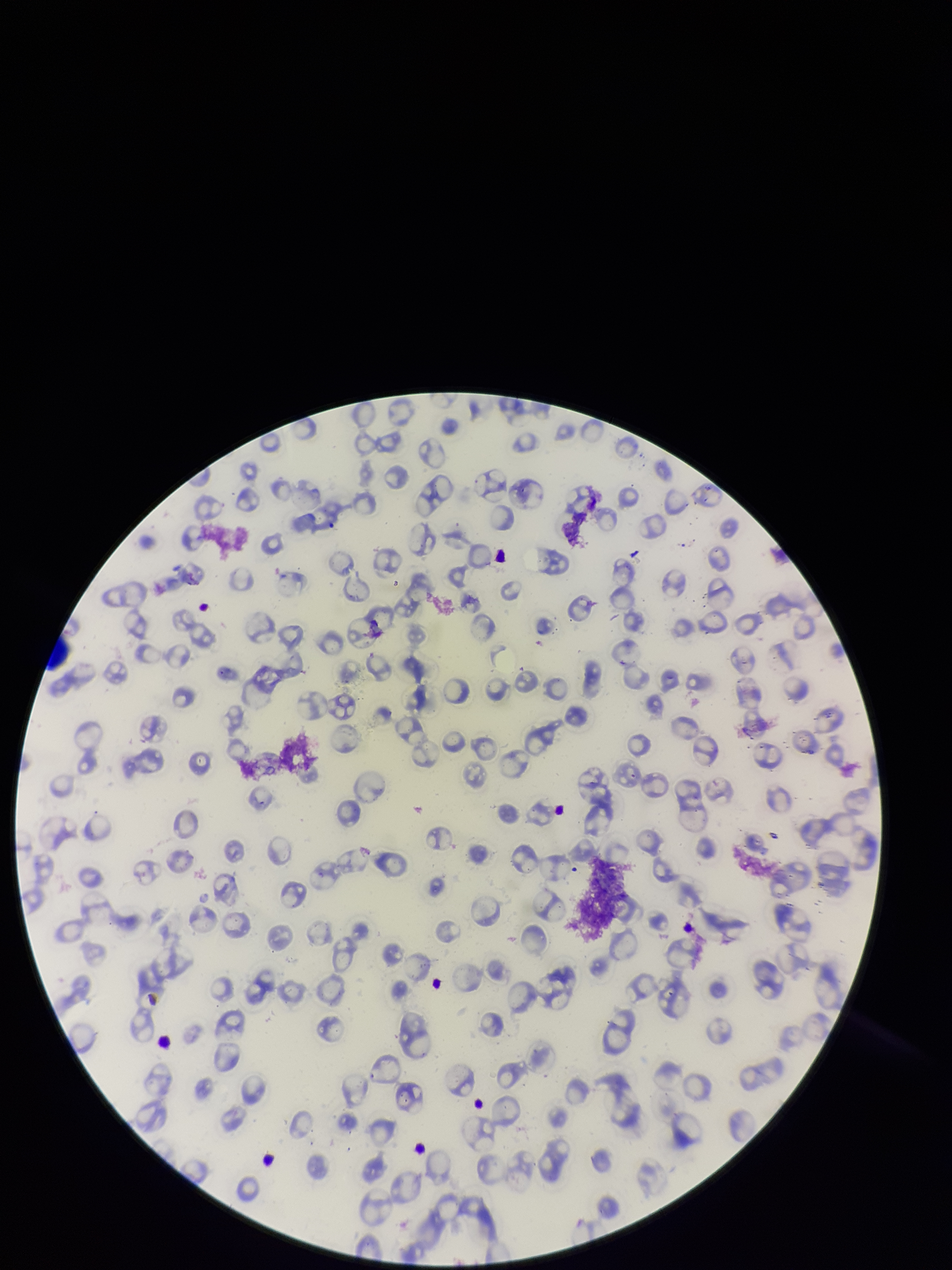
Summary:
  - Image size: 952×1270 pixels
  - Red blood cell count: 83
  - Species reported for this patient: Plasmodium falciparum
  - Preparation: thin blood smear
  - Patient malaria status: positive
  - Parasitized red blood cell count: 0
  - Stain: Giemsa
  - Parasitized red blood cells: none detected
  - Capture: smartphone photograph through the microscope eyepiece
  - Field of view: one from this slide